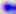

identification = Toxoplasma gondii
modality = photomicrograph
magnification = 400x